State which parasite is depicted.
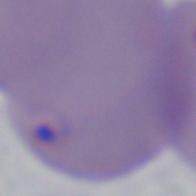
Babesia.

magnification: 1000x
modality: photomicrograph